State which parasite is depicted.
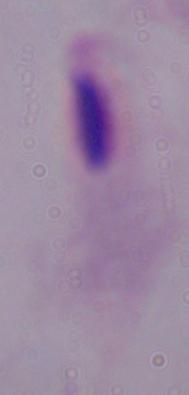

This is a trichomonad.

{
  "magnification": "1000x",
  "modality": "micrograph"
}